State the blood parasite species.
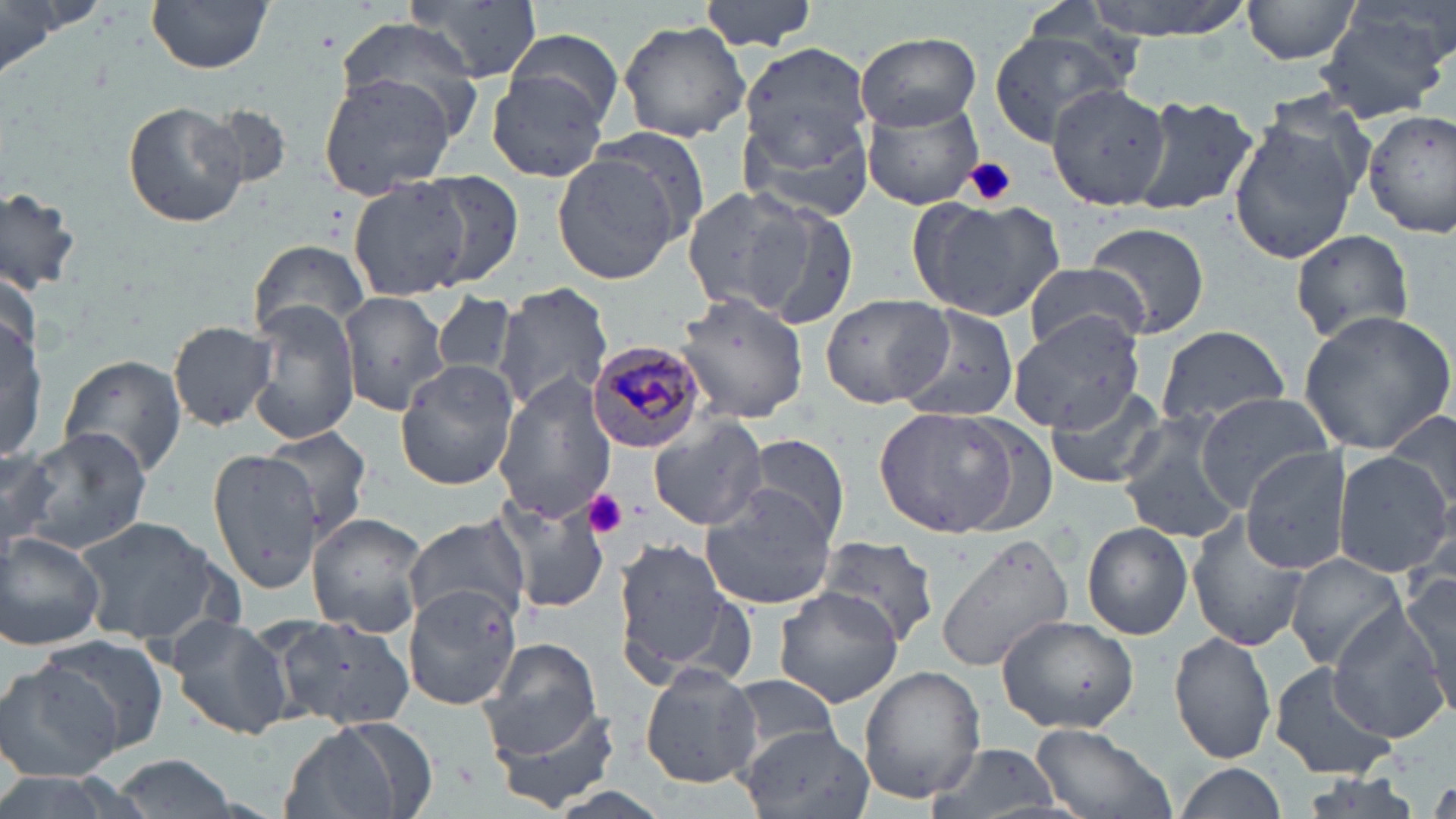

Plasmodium malariae.

Summary:
  - Coordinate format: approximate bounding boxes as named x1/y1/x2/y2 corners in pixels
  - Uninfected red blood cell locations: (x1=404, y1=0, x2=546, y2=83), (x1=699, y1=0, x2=818, y2=52), (x1=1079, y1=0, x2=1258, y2=41), (x1=1240, y1=0, x2=1363, y2=66), (x1=0, y1=1, x2=90, y2=78), (x1=147, y1=1, x2=274, y2=74), (x1=1315, y1=11, x2=1449, y2=121), (x1=332, y1=16, x2=484, y2=125), (x1=617, y1=19, x2=750, y2=143), (x1=504, y1=29, x2=624, y2=127), (x1=988, y1=30, x2=1125, y2=141), (x1=853, y1=32, x2=980, y2=130), (x1=737, y1=40, x2=873, y2=171), (x1=485, y1=70, x2=610, y2=183), (x1=317, y1=73, x2=459, y2=198), (x1=1040, y1=82, x2=1173, y2=210), (x1=740, y1=85, x2=876, y2=225), (x1=1129, y1=94, x2=1259, y2=216), (x1=860, y1=97, x2=985, y2=210), (x1=121, y1=99, x2=251, y2=227), (x1=1364, y1=107, x2=1456, y2=240), (x1=1227, y1=112, x2=1363, y2=264), (x1=550, y1=152, x2=684, y2=285), (x1=410, y1=171, x2=525, y2=287), (x1=349, y1=177, x2=474, y2=300), (x1=0, y1=183, x2=85, y2=297), (x1=681, y1=184, x2=820, y2=321), (x1=909, y1=196, x2=1065, y2=320), (x1=755, y1=201, x2=861, y2=332), (x1=1084, y1=222, x2=1209, y2=338), (x1=1290, y1=228, x2=1414, y2=347), (x1=249, y1=239, x2=370, y2=343), (x1=1022, y1=263, x2=1151, y2=353), (x1=494, y1=283, x2=612, y2=416), (x1=337, y1=291, x2=448, y2=415), (x1=429, y1=291, x2=518, y2=384), (x1=669, y1=292, x2=812, y2=425), (x1=820, y1=293, x2=954, y2=407), (x1=251, y1=301, x2=362, y2=445), (x1=1, y1=303, x2=47, y2=466), (x1=894, y1=304, x2=1022, y2=425), (x1=1296, y1=308, x2=1456, y2=455), (x1=1009, y1=313, x2=1147, y2=431), (x1=168, y1=320, x2=277, y2=431), (x1=1155, y1=325, x2=1291, y2=428), (x1=58, y1=355, x2=188, y2=481), (x1=395, y1=359, x2=518, y2=490), (x1=494, y1=375, x2=618, y2=526), (x1=1044, y1=383, x2=1167, y2=489), (x1=1195, y1=391, x2=1339, y2=507), (x1=875, y1=407, x2=1033, y2=538), (x1=1384, y1=408, x2=1456, y2=520), (x1=1117, y1=409, x2=1247, y2=548), (x1=649, y1=416, x2=769, y2=531), (x1=18, y1=427, x2=153, y2=554), (x1=264, y1=427, x2=372, y2=540), (x1=741, y1=434, x2=850, y2=544), (x1=0, y1=442, x2=60, y2=552), (x1=206, y1=447, x2=327, y2=592), (x1=1240, y1=447, x2=1354, y2=574), (x1=1333, y1=450, x2=1451, y2=576), (x1=485, y1=491, x2=608, y2=618), (x1=700, y1=491, x2=840, y2=611), (x1=1185, y1=513, x2=1313, y2=653), (x1=306, y1=514, x2=429, y2=638), (x1=403, y1=515, x2=530, y2=626), (x1=77, y1=516, x2=224, y2=647), (x1=1083, y1=522, x2=1193, y2=639), (x1=935, y1=532, x2=1075, y2=674), (x1=1, y1=533, x2=105, y2=651), (x1=814, y1=537, x2=941, y2=650), (x1=614, y1=540, x2=739, y2=679), (x1=1287, y1=552, x2=1408, y2=670), (x1=627, y1=557, x2=748, y2=784), (x1=1399, y1=571, x2=1456, y2=699), (x1=404, y1=583, x2=525, y2=710), (x1=774, y1=586, x2=904, y2=709), (x1=1332, y1=610, x2=1454, y2=742), (x1=269, y1=611, x2=417, y2=747), (x1=996, y1=615, x2=1139, y2=733), (x1=163, y1=616, x2=293, y2=741), (x1=1169, y1=630, x2=1278, y2=764), (x1=37, y1=634, x2=170, y2=754), (x1=481, y1=637, x2=603, y2=758), (x1=1267, y1=661, x2=1399, y2=780), (x1=0, y1=662, x2=124, y2=783), (x1=639, y1=664, x2=763, y2=788), (x1=859, y1=666, x2=985, y2=804), (x1=728, y1=675, x2=845, y2=762), (x1=488, y1=699, x2=623, y2=815), (x1=279, y1=721, x2=427, y2=819), (x1=1028, y1=724, x2=1175, y2=819), (x1=740, y1=725, x2=872, y2=819), (x1=928, y1=742, x2=1062, y2=819), (x1=107, y1=753, x2=245, y2=819), (x1=1171, y1=763, x2=1284, y2=819), (x1=1297, y1=773, x2=1426, y2=819)
  - Plasmodium malariae-infected red blood cell locations: (x1=586, y1=338, x2=706, y2=452)
  - Platelet locations: (x1=963, y1=157, x2=1017, y2=207), (x1=583, y1=488, x2=629, y2=538)
  - Modality: optical microscopy
  - Preparation: thin blood film
  - Image size: 1456×819 pixels
  - Stain: May-Grünwald-Giemsa
  - Field of view: one of a larger specimen
  - Magnification: 1000x